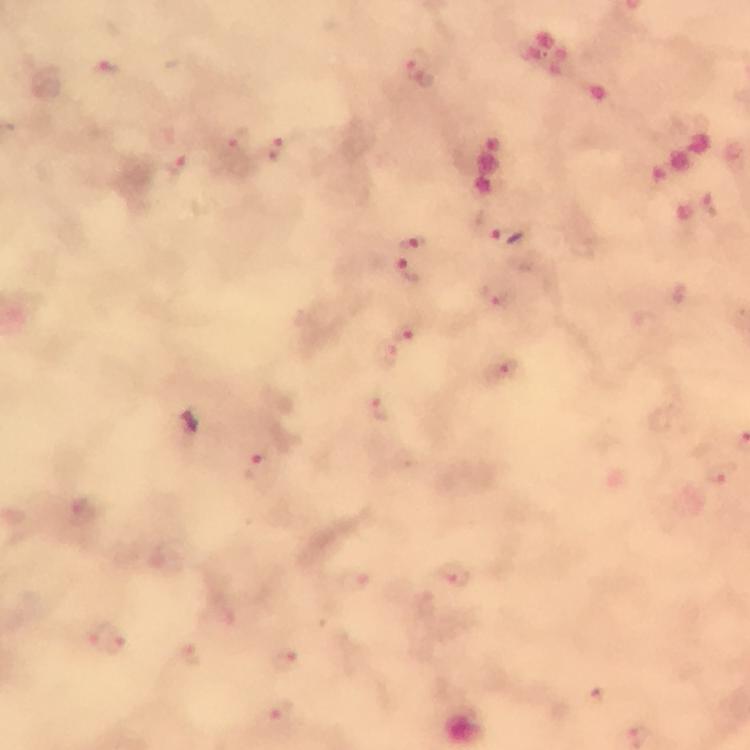
{
  "magnification": "100x",
  "capture": "smartphone photograph through a microscope",
  "preparation": "thick smear",
  "cropped_from": "one field of view",
  "stain": "Giemsa",
  "plasmodium_parasite_locations": "approximate centers as (x, y) in pixels: (418, 64), (107, 68), (237, 139), (275, 149), (173, 163), (493, 227), (413, 241), (411, 273), (498, 297), (412, 332), (380, 357), (502, 370), (380, 410), (258, 467), (722, 476), (81, 513), (457, 573), (356, 582), (108, 639), (190, 652), (288, 656), (281, 712)",
  "immersion_oil": "applied",
  "context": "from a diagnostic examination for malaria",
  "image_size": "750×750 pixels"
}